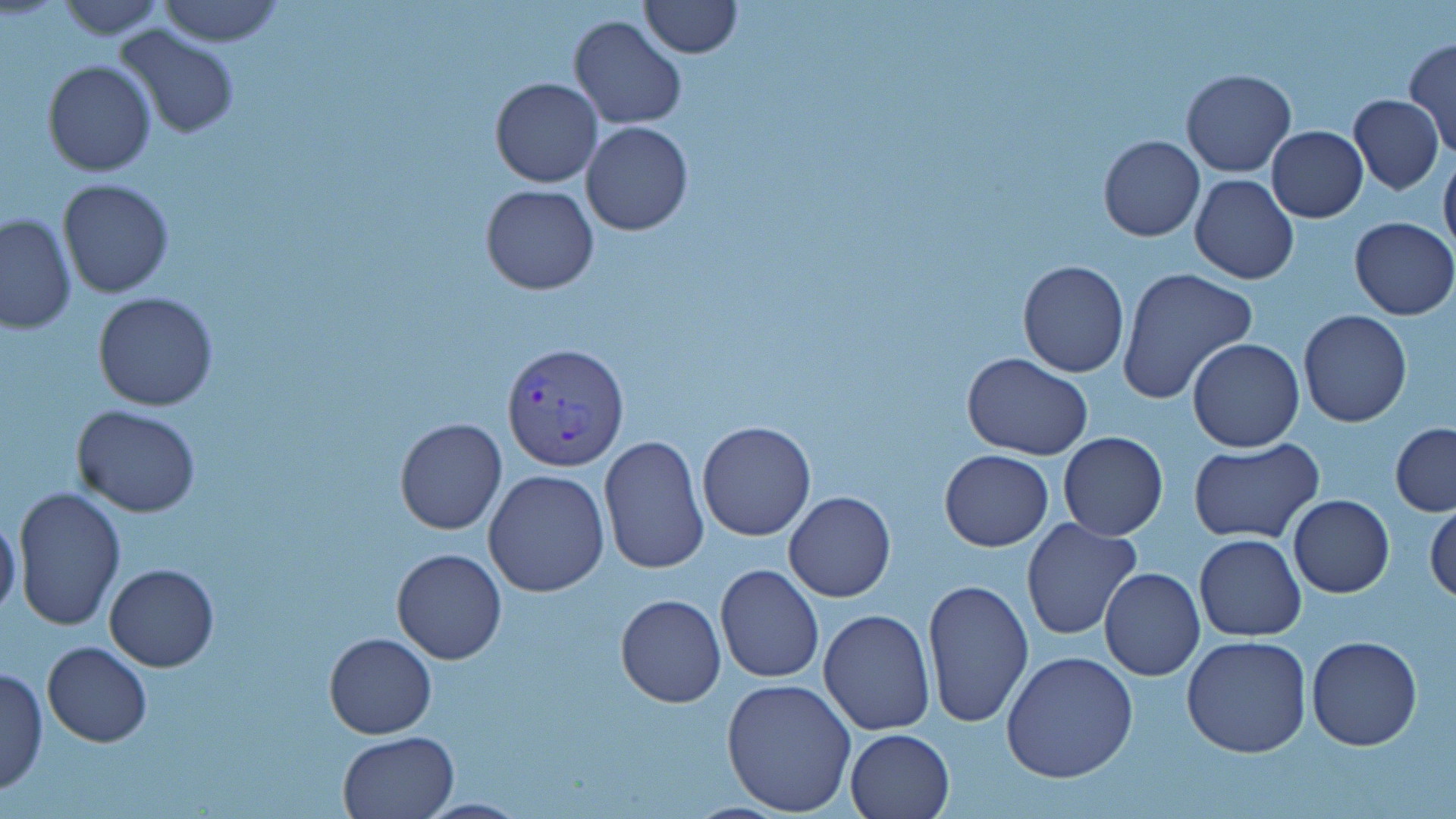
Summary:
  - Coordinate format: approximate bounding boxes as (x1,y1)-(x2,y2) corner pairs in pixels
  - Uninfected red blood cell locations: (56,0)-(167,38), (156,0)-(286,46), (639,1)-(741,58), (568,14)-(688,129), (111,27)-(240,140), (1404,38)-(1456,157), (42,60)-(157,177), (1181,68)-(1296,177), (490,77)-(602,188), (1349,94)-(1444,195), (581,121)-(695,235), (1266,125)-(1368,221), (1098,136)-(1205,242), (1439,152)-(1456,259), (1191,174)-(1299,286), (57,178)-(173,298), (480,183)-(599,295), (0,214)-(75,335), (1349,216)-(1456,320), (1017,259)-(1130,378), (1117,267)-(1258,404), (93,291)-(219,410), (1298,310)-(1412,427), (1187,338)-(1304,452), (962,353)-(1093,458), (72,404)-(201,516), (395,418)-(506,535), (697,420)-(816,540), (1390,423)-(1456,516), (1058,432)-(1168,540), (598,433)-(710,577), (1190,440)-(1324,545), (939,449)-(1053,551), (482,469)-(609,598), (12,487)-(124,632), (784,492)-(896,603), (1288,494)-(1393,597), (1426,502)-(1456,604), (0,516)-(22,621), (1020,516)-(1141,641), (1194,535)-(1307,640), (391,548)-(507,664), (104,562)-(219,672), (714,562)-(824,684), (1099,567)-(1205,681), (921,577)-(1034,727), (614,593)-(726,707), (819,608)-(936,736), (324,632)-(437,740), (1181,634)-(1312,757), (1305,637)-(1424,752), (41,641)-(153,747), (1001,650)-(1138,783), (0,666)-(48,798), (721,677)-(856,816), (844,728)-(954,819), (335,732)-(459,819), (414,798)-(531,817)
  - Plasmodium vivax-infected red blood cell locations: (501,341)-(629,474)
  - Slide-level diagnosis: Plasmodium vivax
  - Field of view: one of a larger specimen
  - Modality: optical microscopy
  - Image size: 1456×819 pixels
  - Magnification: 1000x
  - Preparation: thin blood smear
  - Stain: May-Grünwald-Giemsa